Give the preparation type.
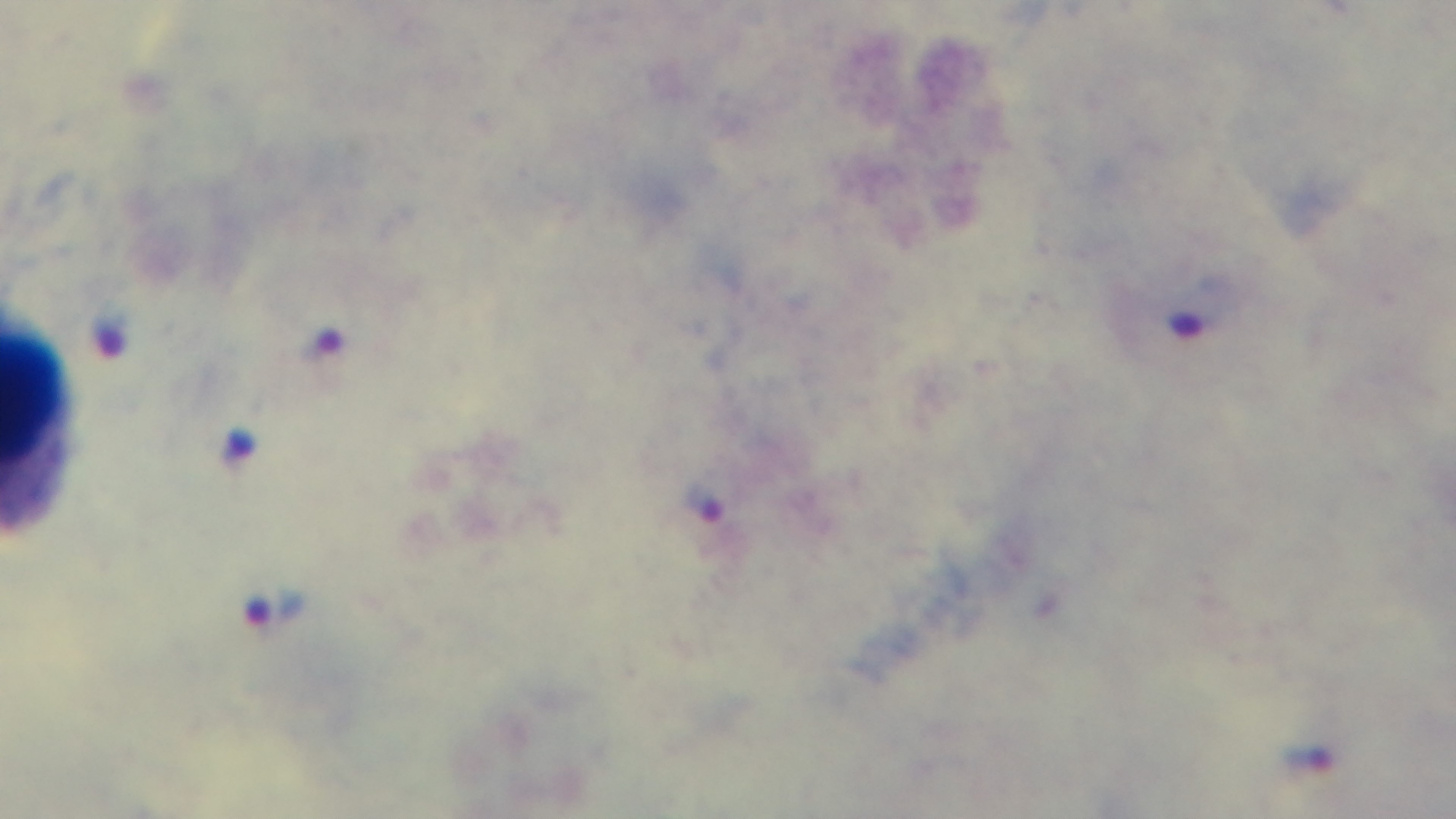

It is a thick blood film.

Malaria status: positive. Mounted 4K digital camera. 100x oil-immersion objective. Light microscopy. Giemsa-stained. Single field of view.